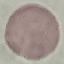
Summary:
  - Malaria status: uninfected
  - Capture: smartphone through the microscope eyepiece
  - Stain: Giemsa
  - Preparation: thin blood film
  - Image type: cell patch, automatically extracted from a larger field of view and resized to 64 × 64 pixels